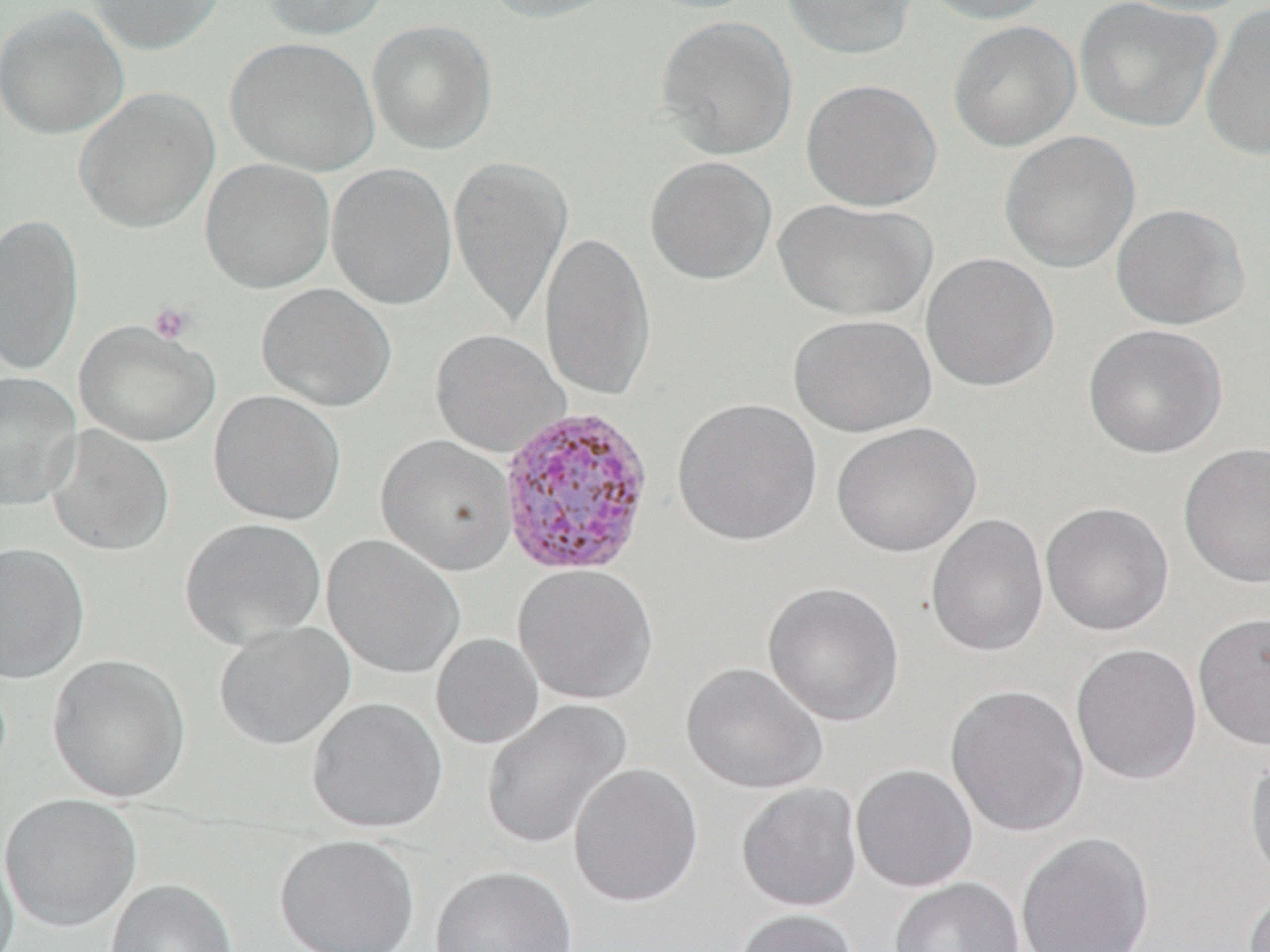
Plasmodium vivax-infected red blood cell locations = approximate bounding boxes as [x1, y1, x2, y2] in pixels: [496, 404, 656, 578]
slide-level diagnosis = Plasmodium vivax
magnification = 1000x
platelet locations = approximate bounding boxes as [x1, y1, x2, y2] in pixels: [149, 302, 196, 345]
stain = May-Grünwald-Giemsa
field of view = one of a larger specimen
modality = light microscopy
uninfected red blood cell locations = approximate bounding boxes as [x1, y1, x2, y2] in pixels: [86, 0, 226, 55], [259, 0, 390, 40], [481, 0, 622, 22], [780, 0, 920, 60], [917, 0, 1058, 25], [1074, 0, 1222, 132], [1110, 0, 1259, 16], [0, 4, 130, 140], [1200, 4, 1270, 162], [655, 15, 798, 160], [366, 19, 498, 154], [948, 20, 1081, 152], [225, 37, 381, 176], [800, 78, 942, 212], [74, 86, 221, 235], [999, 130, 1141, 273], [447, 155, 574, 329], [644, 155, 777, 285], [200, 158, 336, 294], [326, 163, 458, 310], [773, 198, 937, 322], [1111, 203, 1249, 330], [1, 213, 84, 377], [539, 227, 656, 404], [920, 252, 1059, 391], [256, 283, 397, 412], [789, 313, 936, 437], [75, 319, 220, 447], [1083, 324, 1228, 460], [430, 328, 570, 458], [0, 371, 82, 511], [209, 389, 347, 525], [672, 396, 824, 546], [831, 421, 982, 557], [46, 425, 175, 556], [376, 435, 517, 576], [1178, 442, 1270, 589], [1040, 501, 1174, 636], [926, 512, 1050, 658], [180, 517, 326, 650], [322, 534, 466, 679], [0, 542, 90, 684], [513, 564, 658, 705], [763, 581, 905, 727], [1192, 611, 1270, 750], [213, 621, 355, 749], [431, 633, 544, 749], [1070, 643, 1203, 785], [47, 653, 191, 804], [681, 662, 828, 794], [945, 684, 1089, 838], [307, 697, 448, 834], [481, 699, 633, 851], [1244, 744, 1270, 890], [568, 762, 704, 908], [850, 764, 979, 892], [736, 782, 863, 912], [1, 794, 141, 931], [1015, 832, 1154, 952], [0, 833, 20, 952], [274, 833, 420, 952], [430, 865, 578, 952], [889, 877, 1024, 952], [105, 878, 238, 952], [1243, 886, 1270, 952], [732, 908, 859, 952]
preparation = thin blood film
image size = 1270×952 pixels